State which parasite is depicted.
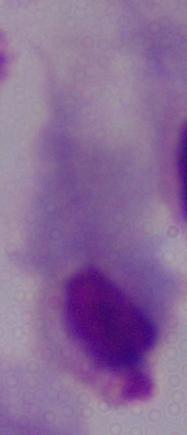

This is a trichomonad.

Summary:
  - Modality: micrograph
  - Magnification: 1000x